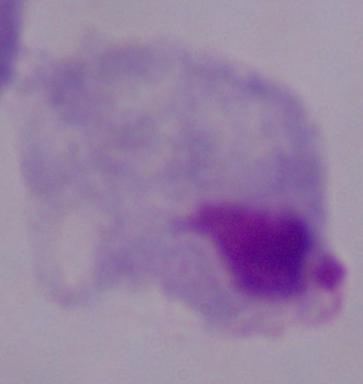

{
  "identification": "trichomonad",
  "magnification": "1000x",
  "modality": "photomicrograph"
}